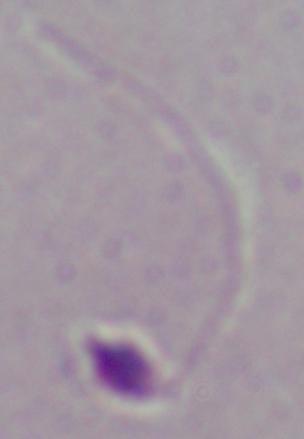

Photomicrograph. Captured at 1000x magnification. A Leishmania parasite is seen.